Report the malaria status of this cell.
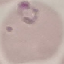

It is parasitized.

Summary:
  - Image type: automatically extracted cell patch, resized to 64 × 64 pixels
  - Preparation: thin blood film
  - Capture: smartphone camera at the microscope eyepiece
  - Stain: Giemsa